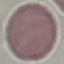

Result: no malaria parasites seen. Giemsa-stained preparation. Cell patch, automatically extracted from a larger field of view and resized to 64 × 64 pixels. Thin blood film. Photographed with a smartphone camera at the microscope eyepiece.